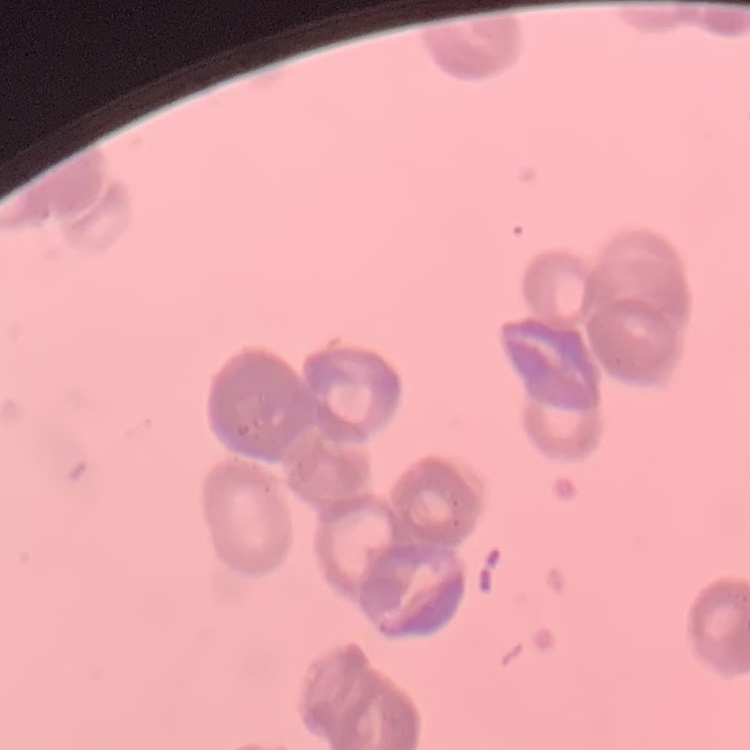
Summary:
  - Erythrocyte morphology: rouleaux formation
  - Stain: Field's or Giemsa
  - Image type: one tile cut from a larger photomicrograph
  - Preparation: thin blood smear